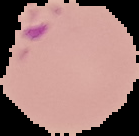

Result: Plasmodium parasites identified. From a thin blood smear. Image is 139×136 pixels. The area outside the segmented cell region is set to black.